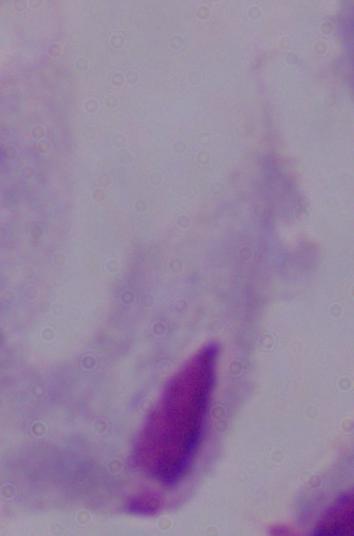

modality = photomicrograph
magnification = 1000x
identification = trichomonad